Assess this cell for malaria.
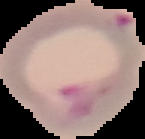
Parasitized.

preparation = thin blood smear
image type = segmented cell region with the area outside set to black
image size = 145×139 pixels